Describe the morphology of the red blood cells.
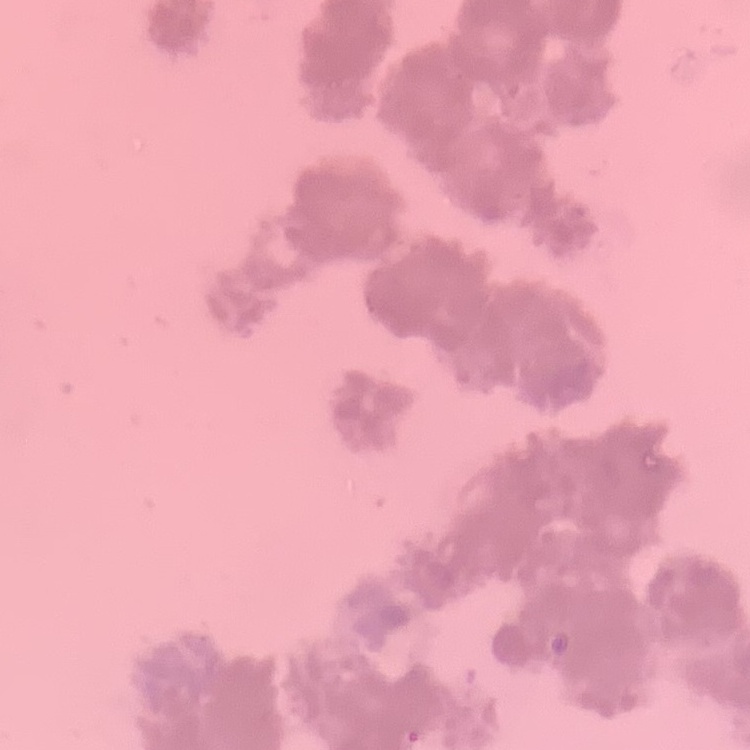
They show rouleaux formation.

stain = Field's or Giemsa
preparation = thin peripheral smear
image type = one tile cut from a larger photomicrograph